Assess this cell for malaria.
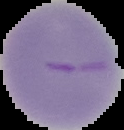

It is parasitized.

Summary:
  - Image size: 124×130 pixels
  - Preparation: thin blood film
  - Image type: segmented cell region on a black background